Identify the preparation type.
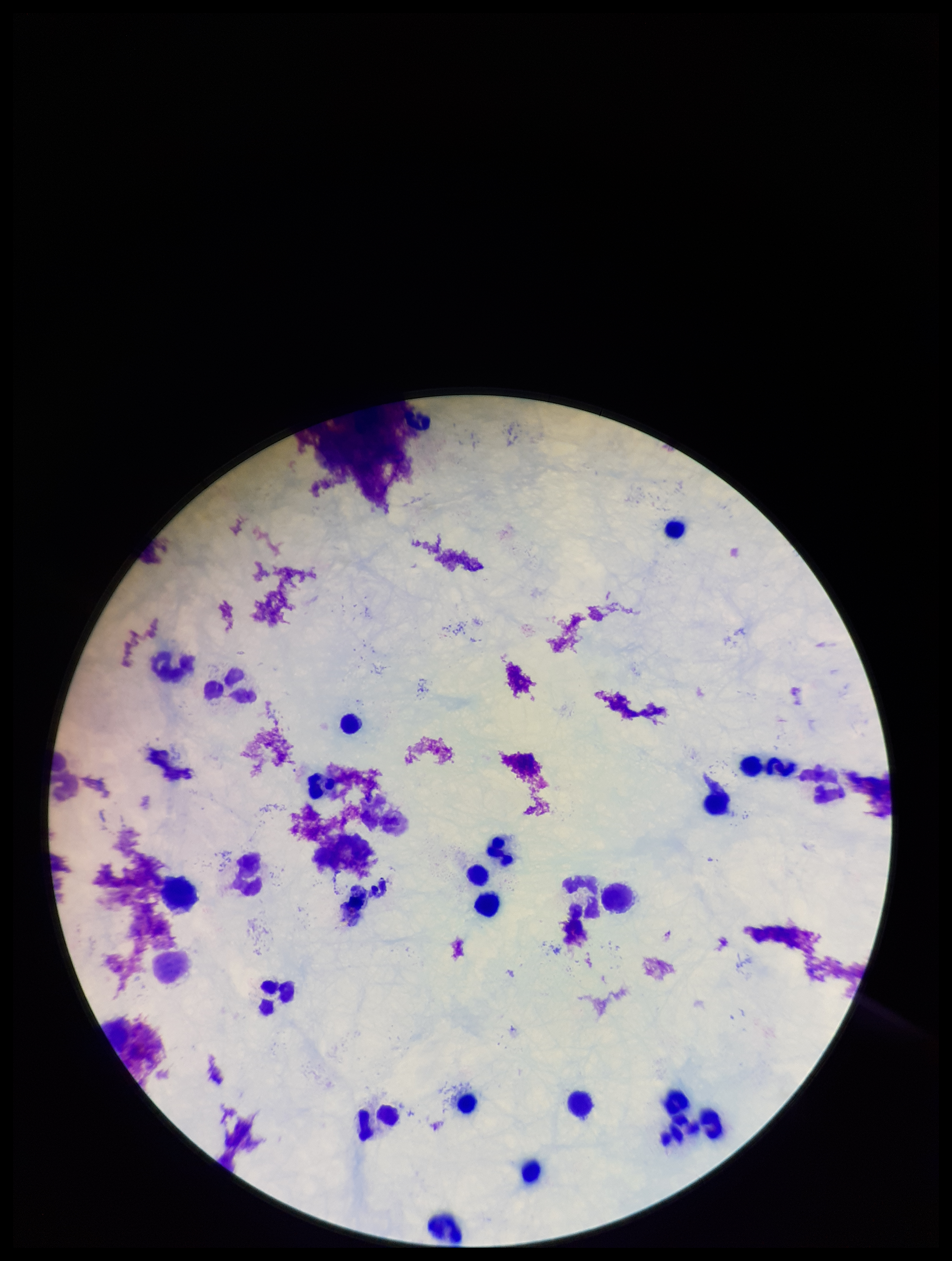

Thick.

One field from this slide. Parasite count: 0. Leukocyte count: 25. Stained with Giemsa. Plasmodium parasites: none detected. Patient malaria status: negative. Image is 952×1261 pixels. Photographed through the microscope eyepiece with a smartphone camera.